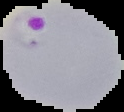

Image is 124×112 pixels. From a thin blood smear. Result: malaria parasites detected. Segmented cell region on a black background.